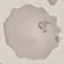
malaria status = uninfected
preparation = thin blood film
stain = Giemsa
capture = smartphone camera at the microscope eyepiece
image type = cell patch, automatically extracted from a larger field of view and resized to 64 × 64 pixels